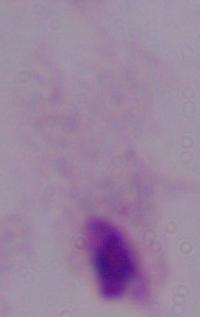

{
  "magnification": "1000x",
  "modality": "micrograph",
  "identification": "trichomonad"
}